State which parasite is depicted.
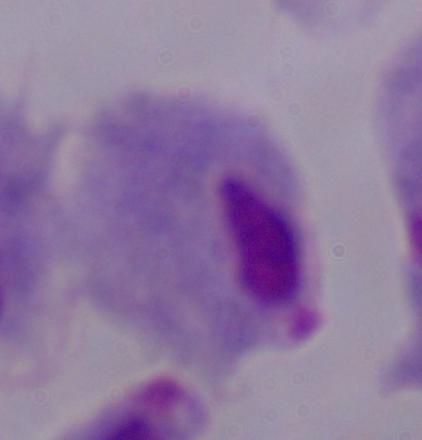
This is a trichomonad.

magnification = 1000x
modality = micrograph